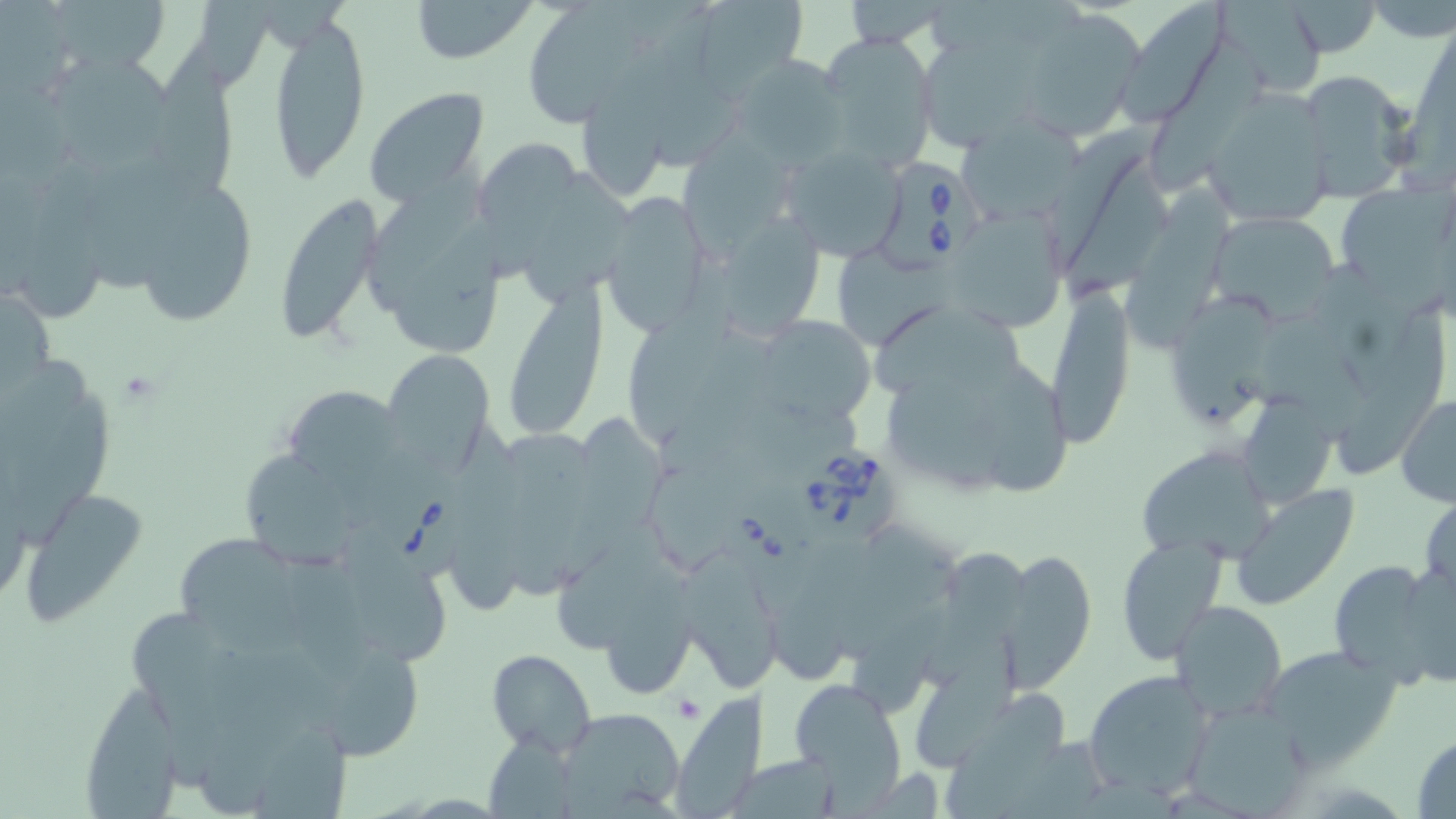
slide-level diagnosis = Babesia divergens
modality = light microscopy
uninfected red blood cell locations = approximate bounding boxes as (x1,y1)-(x2,y2) corner pairs in pixels: (408,0)-(538,64), (685,0)-(813,97), (1285,0)-(1381,57), (531,1)-(644,127), (840,1)-(953,49), (1116,1)-(1228,124), (1018,12)-(1146,142), (265,14)-(370,183), (817,32)-(940,170), (143,35)-(240,208), (577,36)-(682,199), (921,36)-(1041,155), (1146,37)-(1270,202), (50,50)-(178,174), (733,54)-(851,165), (1295,68)-(1418,198), (364,87)-(488,208), (1202,89)-(1337,226), (1034,132)-(1154,279), (684,134)-(799,264), (474,140)-(583,285), (780,145)-(909,263), (26,160)-(112,324), (363,162)-(487,314), (526,172)-(647,307), (1340,176)-(1456,312), (1123,179)-(1237,366), (138,186)-(258,327), (271,194)-(384,348), (600,194)-(712,338), (948,208)-(1066,334), (720,211)-(828,348), (1207,213)-(1338,323), (501,283)-(610,441), (1045,285)-(1134,446), (630,289)-(735,442), (873,296)-(1032,410), (1165,296)-(1288,437), (1258,313)-(1382,445), (1330,313)-(1447,487), (763,319)-(876,428), (385,350)-(490,466), (2,355)-(89,485), (967,359)-(1076,502), (289,381)-(404,513), (1396,394)-(1456,507), (556,414)-(677,588), (497,419)-(588,605), (445,424)-(541,619), (1141,446)-(1276,562), (240,453)-(360,570), (19,484)-(149,624), (1230,484)-(1360,611), (1420,488)-(1455,602), (561,510)-(672,667), (174,535)-(310,657), (1116,538)-(1227,664), (998,547)-(1097,692), (681,549)-(781,695), (924,551)-(1029,689), (329,555)-(462,669), (1398,556)-(1456,690), (1329,558)-(1452,687), (850,593)-(952,720), (1169,601)-(1288,721), (310,644)-(435,769), (1261,646)-(1404,770), (486,650)-(596,756), (1083,668)-(1217,799), (790,676)-(906,802), (77,683)-(183,814), (675,693)-(775,819), (943,693)-(1063,819), (551,708)-(688,814), (1410,732)-(1456,818)
platelet locations = approximate bounding boxes as (x1,y1)-(x2,y2) corner pairs in pixels: (671,692)-(703,721)
stain = May-Grünwald-Giemsa
image size = 1456×819 pixels
Babesia divergens-infected red blood cell locations = approximate bounding boxes as (x1,y1)-(x2,y2) corner pairs in pixels: (876,160)-(984,278), (794,444)-(902,546), (381,473)-(469,583), (721,485)-(831,599)
field of view = single
preparation = thin blood film
magnification = 1000x